Describe the morphology of the red blood cells.
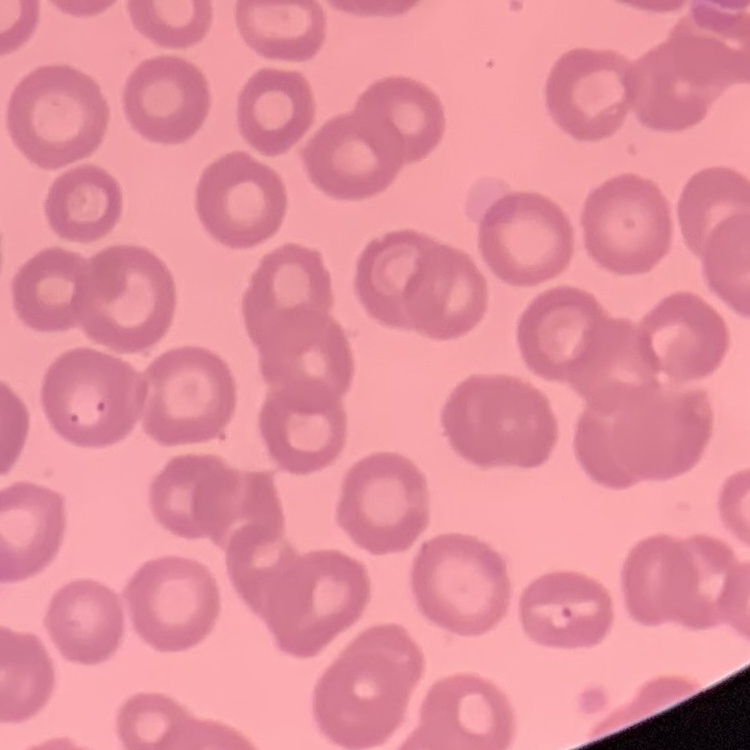

No rouleaux formation.

image type = one tile cut from a larger photomicrograph
stain = Field's or Giemsa
preparation = thin peripheral smear